State the preparation type.
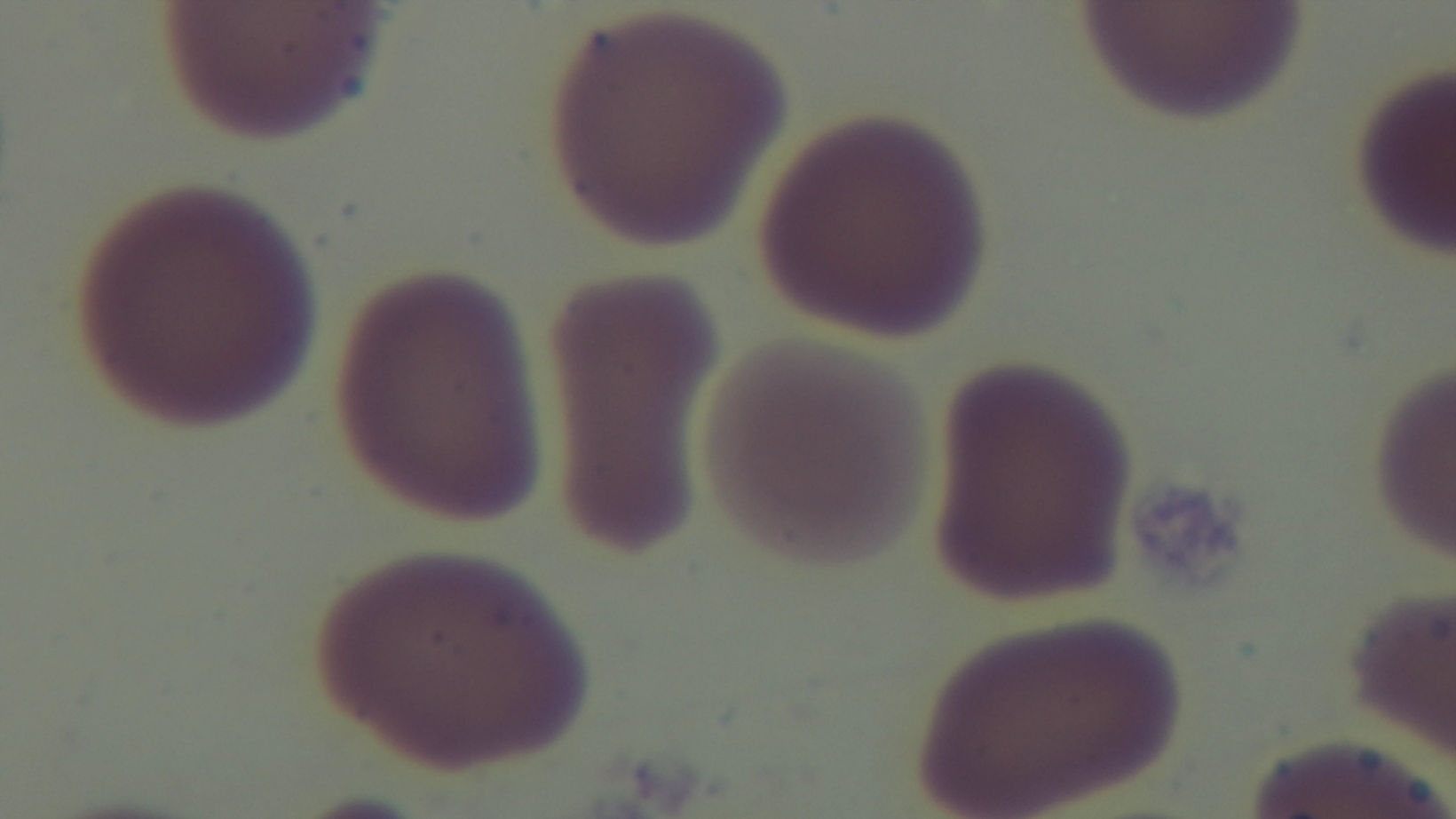
It is a thin blood film.

Summary:
  - Stain: Giemsa
  - Malaria status: negative
  - Capture: mounted 4K digital camera
  - Modality: light microscopy
  - Field of view: single
  - Objective: 100x oil immersion